Classify this cell by malaria status.
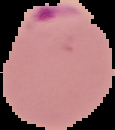
Parasitized.

Image is 115×130 pixels. From a thin blood smear. The area outside the segmented cell region is set to black.